Assess this cell for malaria.
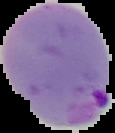

It is parasitized.

{
  "image_size": "115×133 pixels",
  "image_type": "cell region segmented out of the field of view; surrounding area masked to black",
  "preparation": "thin blood smear"
}